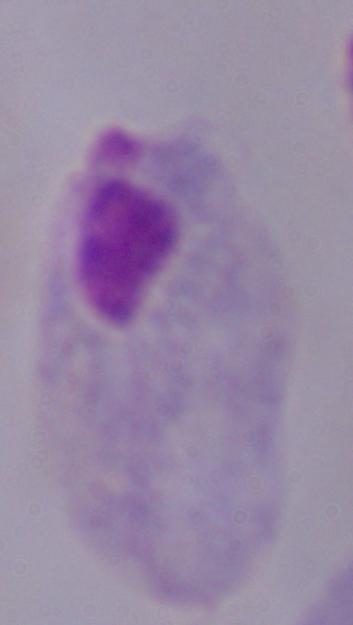
modality = micrograph
identification = trichomonad
magnification = 1000x